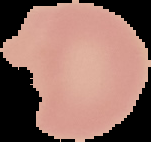

preparation = thin blood smear
image type = cell region segmented out of the field of view; surrounding area masked to black
result = no malaria parasites seen
image size = 151×142 pixels